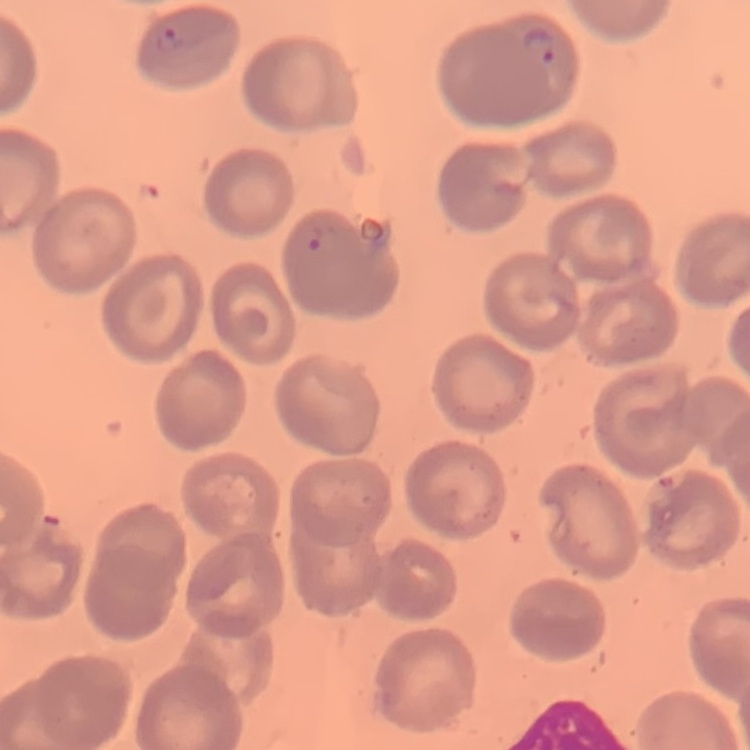

red blood cell morphology = no rouleaux formation
stain = Field's or Giemsa
preparation = thin peripheral smear
image type = one tile cut from a larger photomicrograph